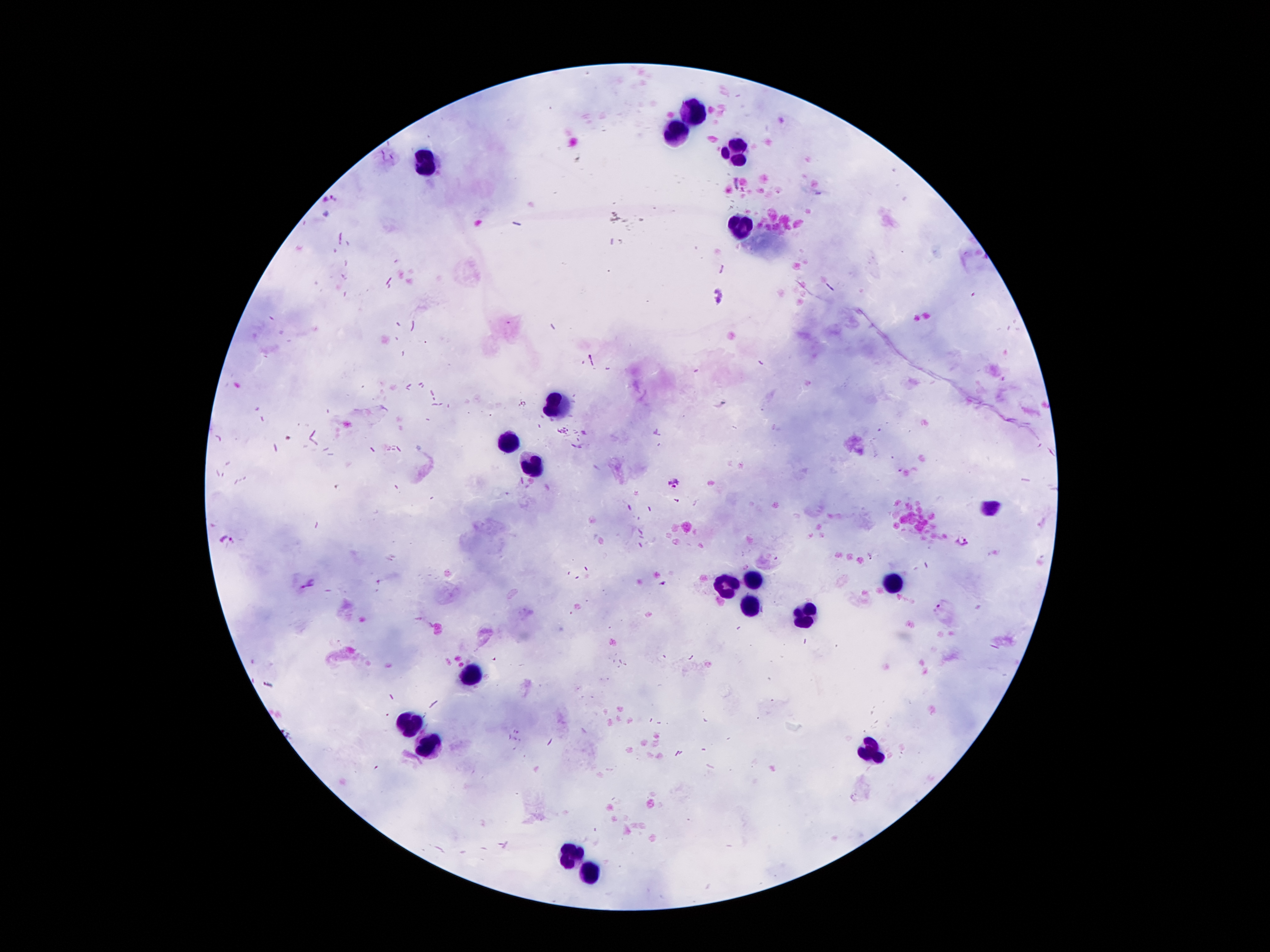

coordinate format = approximate centers as (x, y) in pixels
leukocyte locations = (696, 113), (676, 133), (732, 150), (427, 163), (741, 228), (556, 402), (506, 445), (532, 465), (991, 508), (896, 579), (754, 581), (724, 583), (748, 607), (803, 616), (472, 672), (413, 721), (427, 749), (874, 752), (573, 853), (594, 872)
malaria parasite locations = (674, 482), (227, 539), (962, 541), (309, 583)
magnification = 100x
patient malaria status = infected with Plasmodium falciparum
capture = smartphone through the microscope eyepiece
stain = Giemsa
preparation = thick peripheral-blood smear
field of view = single
image size = 1270×952 pixels